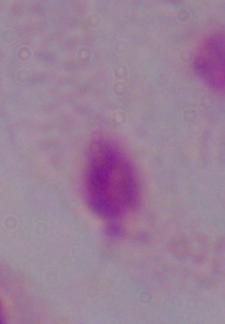 A trichomonad is shown. Photomicrograph. Captured at 1000x magnification.